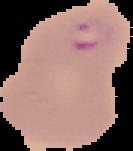
preparation = thin blood smear
malaria status = parasitized
image type = cell region segmented out of the field of view; surrounding area masked to black
image size = 133×151 pixels